Assess for malaria.
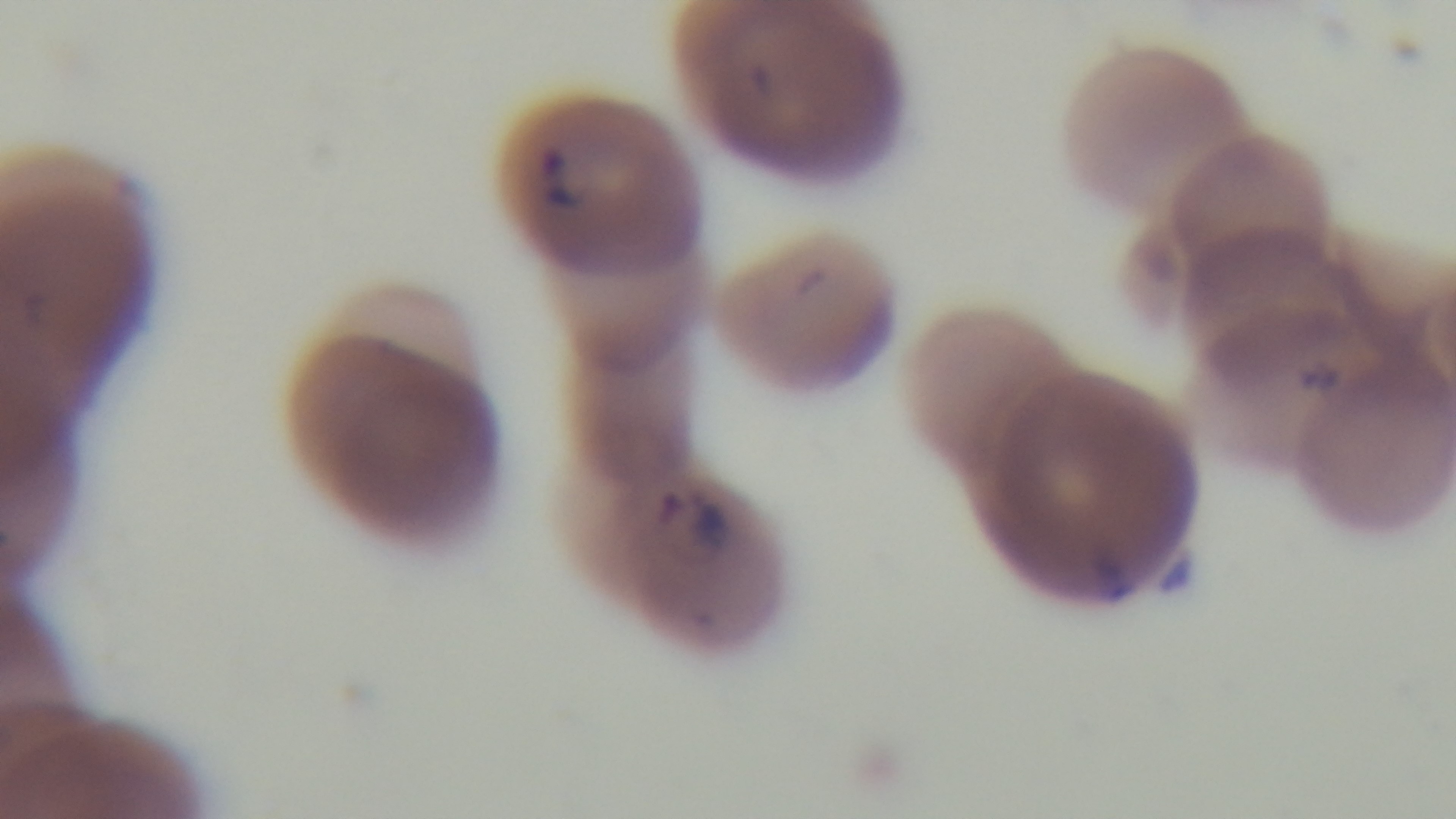

It is infected.

Summary:
  - Preparation: thin smear
  - Field of view: one from the slide
  - Stain: Giemsa
  - Objective: 100x oil immersion
  - Modality: light microscopy
  - Capture: mounted 4K digital camera